Assess this cell for malaria.
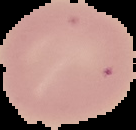
Uninfected.

From a thin blood film. Image is 136×130 pixels. Cell region segmented out of the field of view; the surrounding area is masked to black.